Comment on the morphology of the red blood cells.
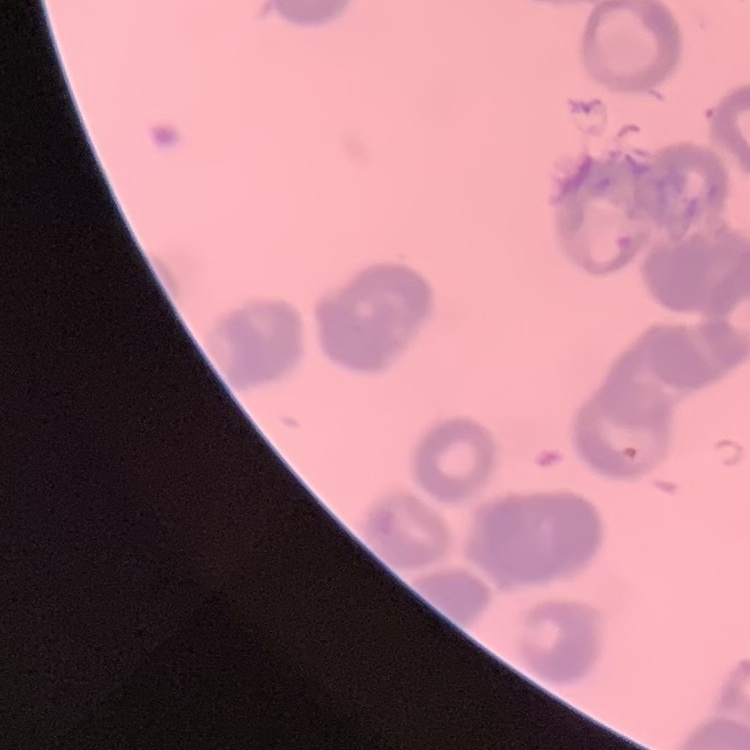

Rouleaux formation.

Thin blood smear. One tile cut from a larger photomicrograph. Field's or Giemsa stain.